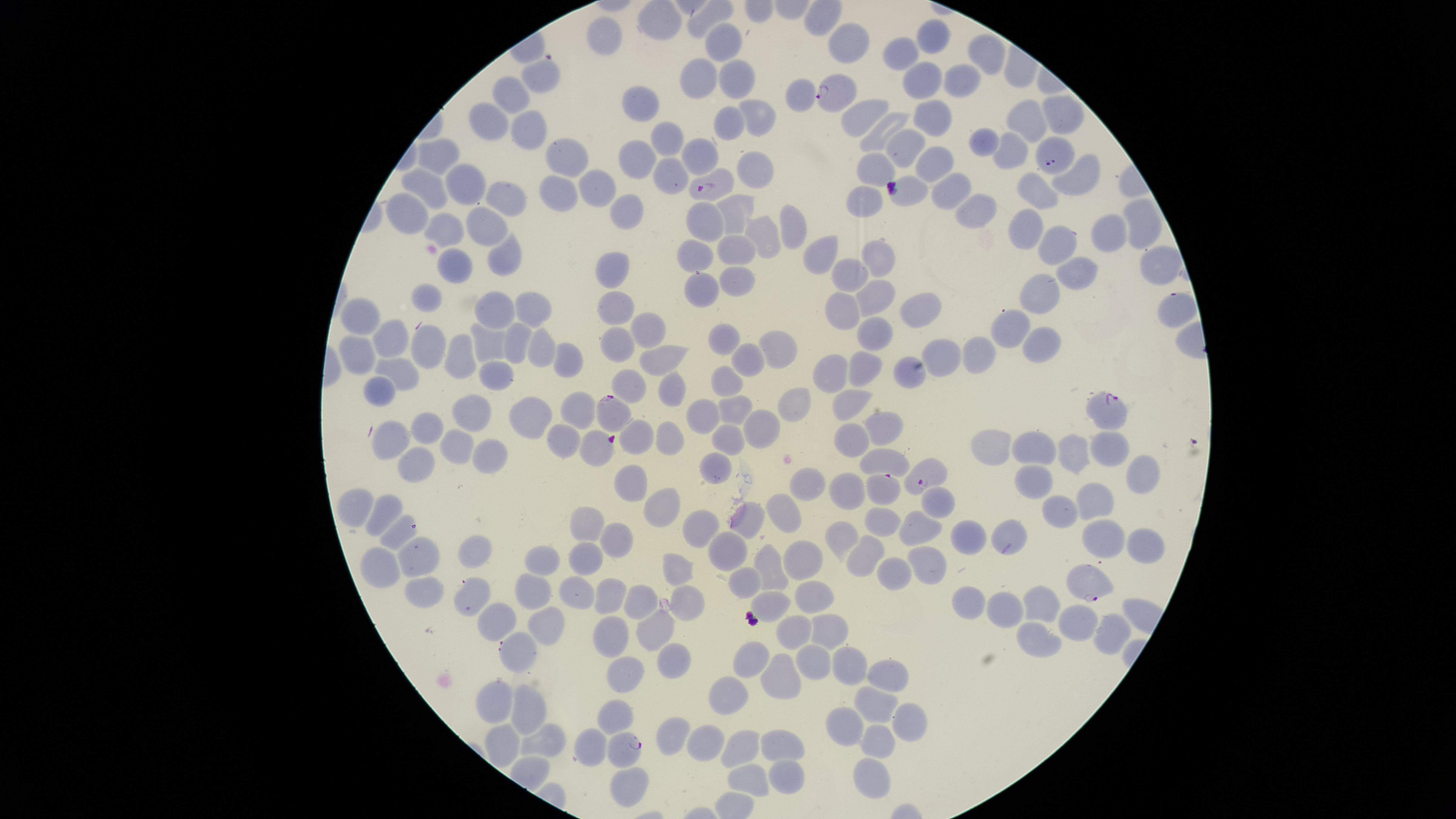

presence = malaria parasites identified
visible region = circular
stain = Giemsa
field of view = single
species = Plasmodium falciparum
preparation = thin blood film
uninfected red blood cells = approximate marker points as (x, y) in pixels: (933, 35), (596, 36), (722, 42), (841, 43), (900, 51), (986, 51), (543, 73), (698, 75), (953, 77), (916, 78), (739, 79), (794, 93), (509, 95), (931, 110), (636, 111), (491, 112), (860, 113), (1021, 113), (1061, 113), (756, 118), (730, 121), (521, 129), (882, 129), (666, 139), (983, 142), (1011, 142), (907, 146), (435, 154), (696, 154), (561, 156), (935, 160), (640, 161), (873, 165), (749, 171), (1075, 172), (668, 176), (475, 181), (950, 185), (1045, 188), (595, 189), (553, 190), (423, 191), (907, 193), (509, 196), (864, 201), (970, 207), (402, 211), (621, 215), (740, 218), (1138, 220), (477, 224), (705, 228), (792, 228), (436, 230), (1024, 231), (1108, 236), (762, 240), (1061, 242), (730, 254), (502, 255), (695, 257), (877, 257), (811, 259), (456, 261), (1154, 265), (613, 269), (1080, 271), (845, 274), (732, 276), (697, 286), (1044, 290), (424, 294), (874, 299), (612, 304), (1176, 304), (497, 309), (839, 309), (528, 313), (914, 313), (359, 317), (647, 323), (1001, 326), (873, 332), (388, 339), (486, 340), (725, 341), (1040, 342), (613, 343), (427, 344), (514, 345), (530, 345), (780, 347), (357, 349), (947, 350), (749, 351), (977, 352), (559, 353), (656, 355), (459, 357), (867, 363), (909, 370), (390, 371), (832, 374), (496, 380), (724, 382), (626, 384), (379, 390), (670, 391), (847, 401), (785, 402), (579, 406), (731, 408), (460, 410), (702, 417), (534, 419), (878, 425), (426, 427), (766, 427), (850, 438), (724, 439), (393, 440), (632, 440), (665, 440), (450, 444), (569, 444), (992, 444), (1034, 446), (593, 447), (1072, 451), (1106, 451), (888, 457), (408, 458), (480, 460), (1140, 466), (710, 467), (1030, 481), (625, 482), (815, 483), (854, 487), (1093, 501), (935, 503), (359, 505), (786, 506), (651, 509), (1061, 510), (386, 511), (586, 517), (746, 518), (879, 522), (920, 525), (398, 532), (691, 534), (1008, 535), (838, 537), (972, 537), (614, 538), (1097, 542), (1141, 545), (724, 551), (475, 553), (867, 555), (418, 559), (544, 559), (584, 560), (796, 561), (381, 564), (674, 564), (767, 565), (924, 565), (889, 571), (741, 579), (528, 586), (577, 589), (427, 590), (602, 594), (472, 595), (966, 597), (815, 601), (687, 602), (1044, 602), (777, 604), (635, 605), (1005, 609), (1076, 624), (499, 625), (653, 627), (831, 627), (545, 628), (789, 628), (613, 634), (1104, 634), (1032, 641), (516, 653), (675, 655), (754, 655), (812, 661), (849, 663), (621, 672), (887, 676), (777, 677), (734, 697), (492, 703), (871, 705), (616, 707), (521, 710), (905, 717), (837, 727), (675, 736), (701, 739), (773, 740), (872, 744), (543, 745), (493, 746), (580, 747), (739, 753), (742, 777), (868, 777), (772, 780), (617, 788)
capture = smartphone photograph through the microscope eyepiece
image size = 1456×819 pixels
parasitized red blood cells = approximate marker points as (x, y) in pixels: (833, 91), (1055, 159), (711, 185), (618, 410), (1110, 411), (920, 472), (883, 490), (1088, 582), (622, 746)